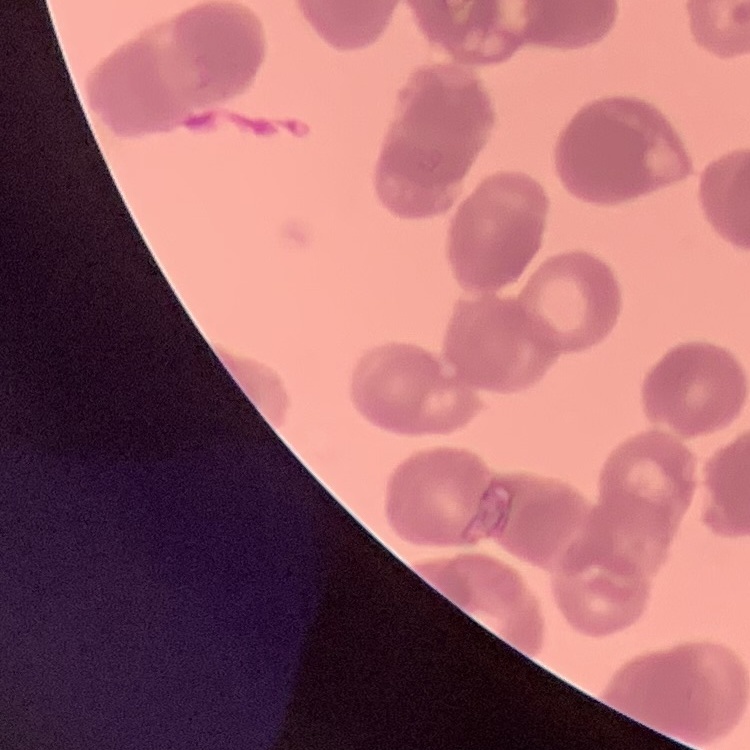

The erythrocytes exhibit rouleaux formation. Field's or Giemsa stain. Thin blood film. One tile cut from a larger photomicrograph.